Locate every Plasmodium parasite.
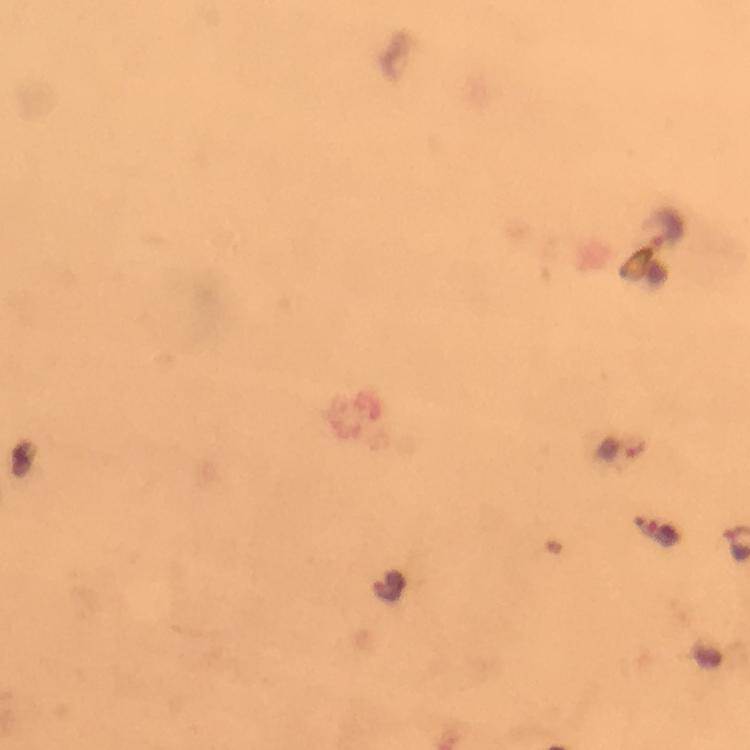

Approximate centers as {x, y} in pixels.
Plasmodium parasites: {664, 229}.

stain = Giemsa
preparation = thick smear
capture = smartphone mounted on the microscope
cropped from = a single field of view
image size = 750×750 pixels
immersion oil = used
magnification = 100x
context = from a malaria diagnostic workup